Comment on the morphology of the red blood cells.
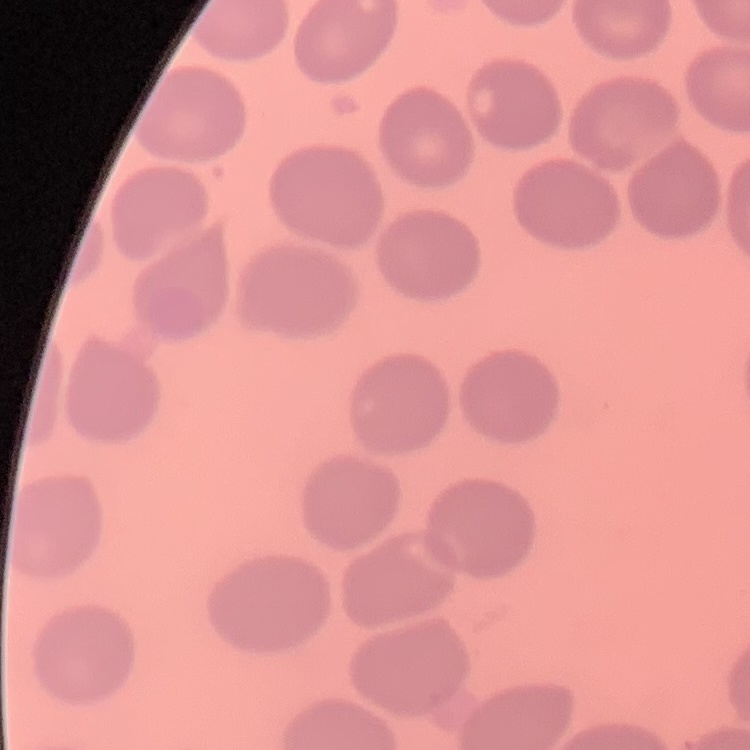

No rouleaux formation.

preparation: thin peripheral smear
stain: Field's or Giemsa
image_type: square crop of a larger photomicrograph